Classify this cell by malaria status.
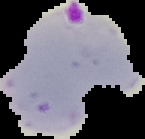
Parasitized.

From a thin blood film. Image is 145×139 pixels. Segmented cell region on a black background.